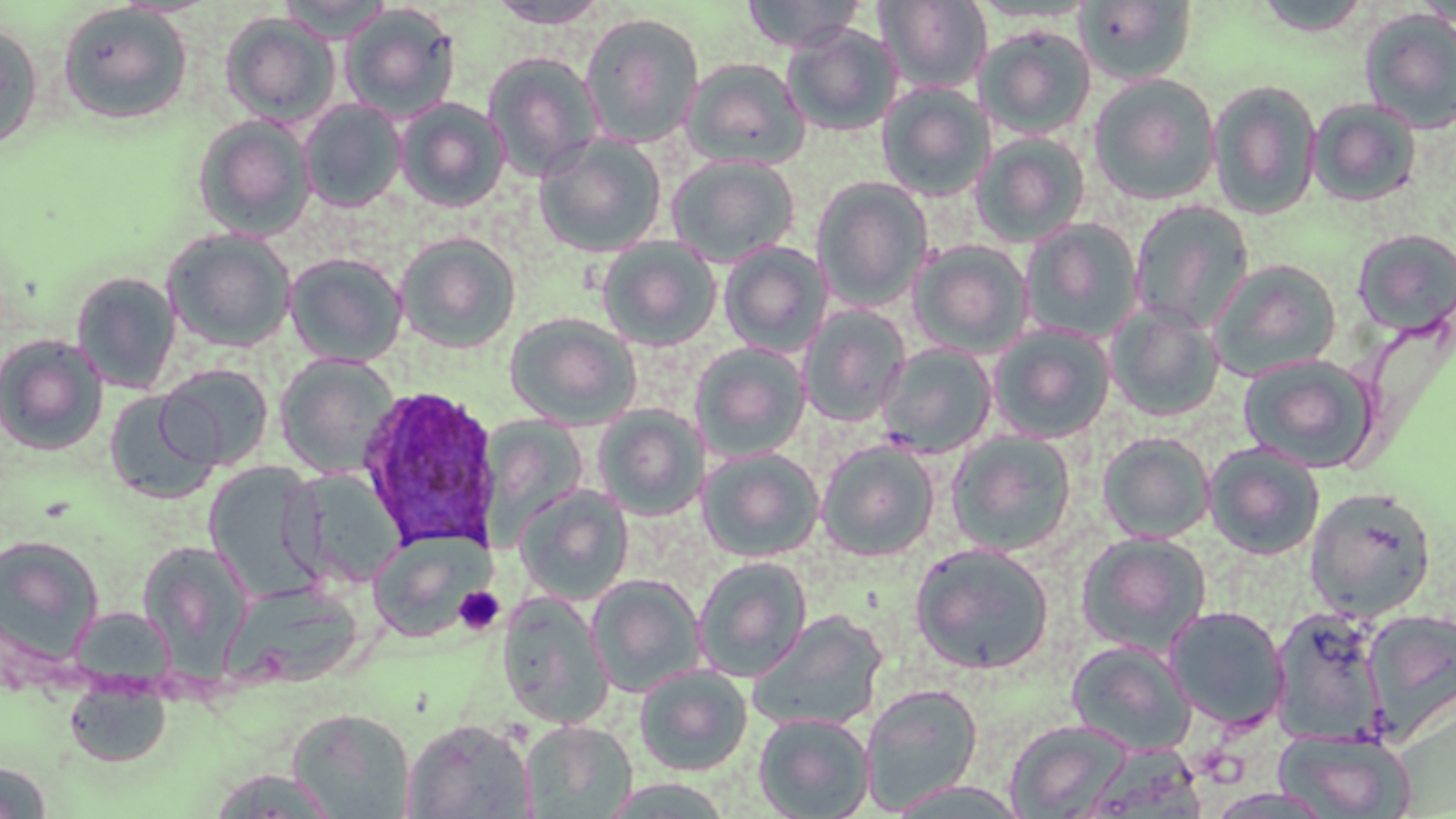

Approximate bounding boxes as (x1, y1, x2, y2) in pixels. Platelet locations: (453, 586, 505, 636). Plasmodium ovale-infected red blood cell locations: (356, 384, 504, 553). Uninfected red blood cell locations: (278, 0, 393, 43), (486, 0, 611, 28), (742, 0, 868, 53), (1249, 0, 1375, 37), (876, 1, 993, 93), (968, 1, 1099, 24), (1075, 1, 1198, 86), (57, 3, 193, 125), (340, 3, 461, 122), (1358, 8, 1456, 133), (580, 11, 705, 148), (220, 13, 340, 126), (0, 22, 44, 152), (782, 23, 902, 137), (975, 25, 1097, 140), (482, 53, 603, 182), (681, 57, 810, 170), (1088, 73, 1222, 206), (1207, 80, 1323, 220), (876, 82, 995, 202), (394, 97, 510, 212), (1308, 98, 1422, 207), (299, 99, 407, 212), (192, 114, 316, 240), (970, 131, 1091, 248), (533, 134, 667, 257), (666, 153, 801, 266), (812, 176, 934, 312), (1128, 199, 1255, 333), (1020, 218, 1144, 344), (162, 228, 297, 352), (1352, 228, 1456, 336), (395, 231, 522, 354), (596, 236, 722, 351), (909, 239, 1034, 359), (718, 242, 833, 358), (284, 252, 408, 366), (1209, 259, 1342, 380), (70, 270, 182, 394), (1105, 303, 1225, 421), (797, 305, 912, 427), (504, 312, 642, 429), (987, 323, 1117, 444), (0, 333, 109, 455), (690, 343, 811, 462), (876, 343, 998, 458), (1237, 353, 1379, 472), (275, 354, 400, 479), (156, 363, 275, 471), (105, 390, 218, 505), (593, 405, 709, 520), (481, 417, 589, 534), (946, 430, 1078, 556), (1097, 431, 1216, 543), (816, 439, 940, 561), (1204, 442, 1325, 560), (697, 447, 825, 562), (203, 461, 323, 600), (286, 468, 404, 589), (514, 485, 634, 605), (1304, 487, 1438, 621), (368, 529, 494, 643), (1076, 532, 1213, 656), (0, 533, 104, 667), (137, 540, 255, 671), (910, 543, 1054, 674), (693, 556, 812, 682), (586, 573, 706, 698), (221, 581, 364, 688), (496, 591, 614, 730), (67, 606, 177, 692), (1163, 606, 1291, 731), (1269, 606, 1391, 745), (1361, 608, 1456, 741), (748, 610, 889, 733), (1066, 640, 1196, 756), (634, 665, 753, 777), (64, 680, 172, 768), (859, 682, 984, 814), (287, 708, 416, 818), (753, 712, 876, 819), (403, 717, 536, 818), (519, 719, 637, 818), (1004, 719, 1134, 818), (1274, 728, 1415, 818), (1082, 742, 1207, 819), (0, 761, 53, 818), (205, 768, 341, 817), (890, 780, 1029, 819), (1204, 788, 1339, 819). Slide-level diagnosis: Plasmodium ovale. One field of a larger specimen. 1000x magnification. Thin blood smear. Optical microscopy. May-Grünwald-Giemsa stain. Image is 1456×819 pixels.